State which parasite is depicted.
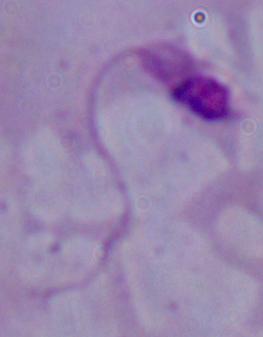
This is Leishmania.

magnification = 1000x
modality = micrograph